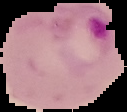 Result: Plasmodium parasites identified. The area outside the segmented cell region is set to black. Image is 127×112 pixels. From a thin blood smear.